Comment on the morphology of the red blood cells.
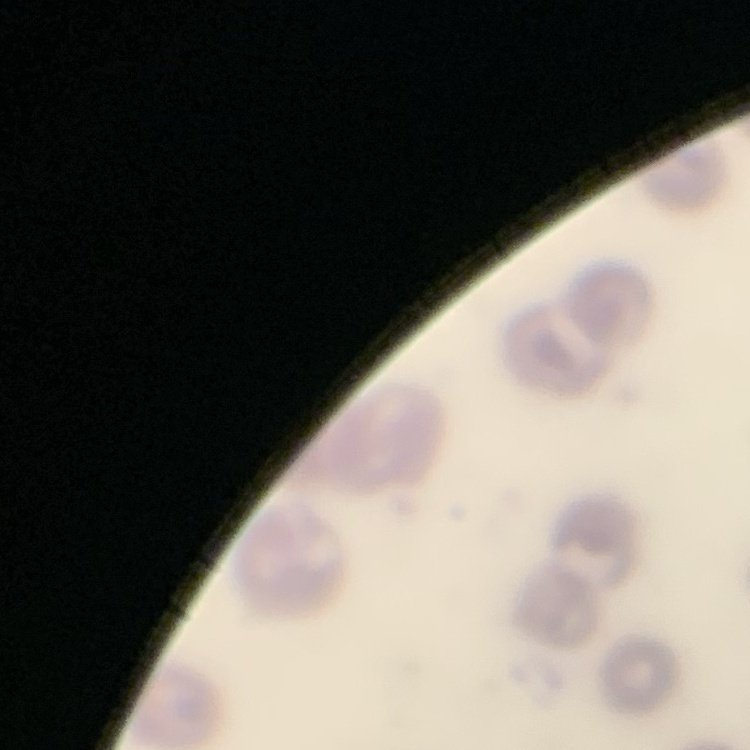
They show no rouleaux formation.

Summary:
  - Preparation: thin blood smear
  - Image type: square crop of a larger photomicrograph
  - Stain: Field's or Giemsa